Assess this cell for malaria.
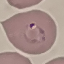

It is parasitized.

capture = smartphone camera at the microscope eyepiece
image type = automatically extracted cell patch, resized to 64 × 64 pixels
stain = Giemsa
preparation = thin blood film